Locate every blood parasite and identify its species.
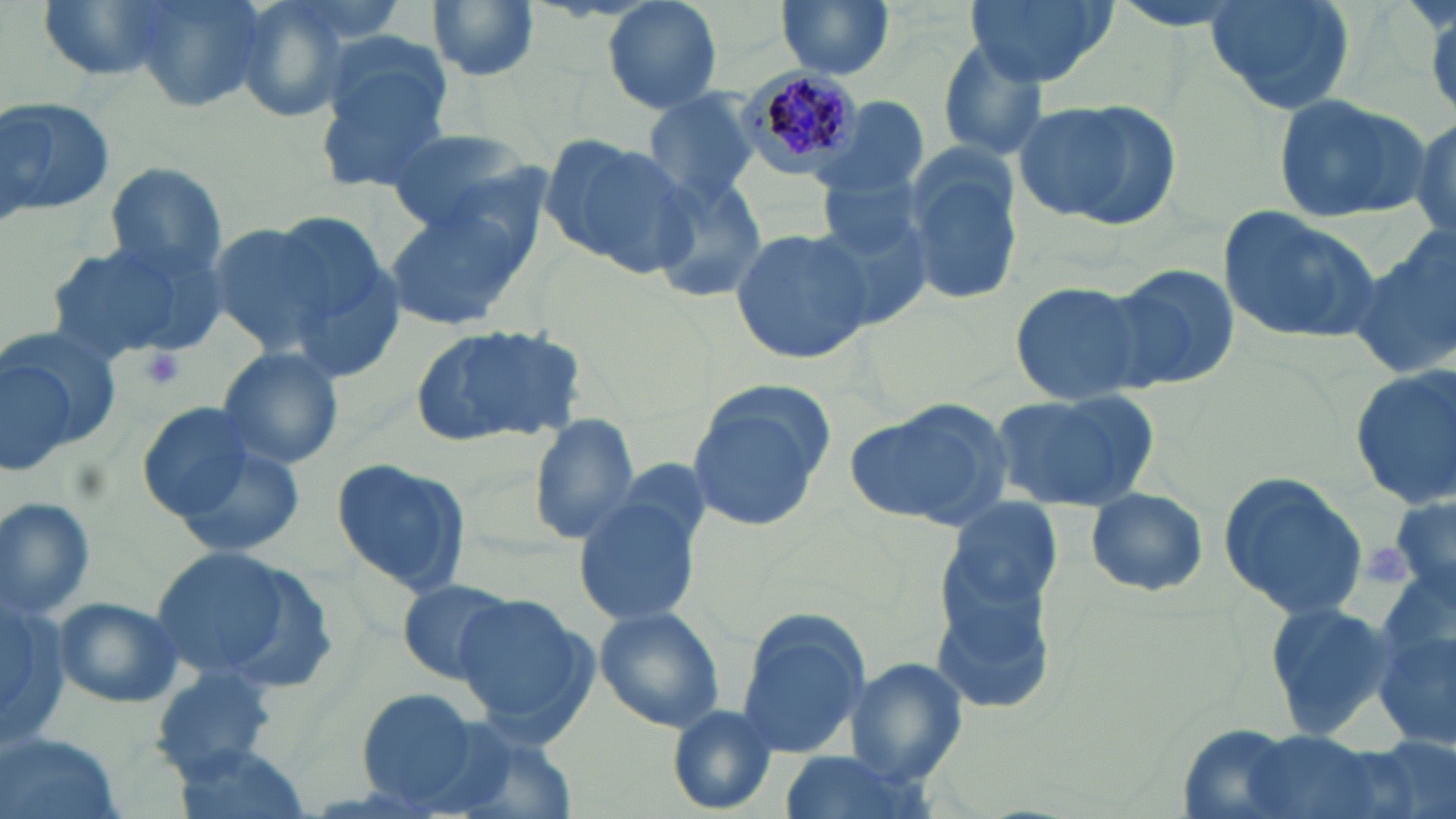

Approximate bounding boxes as (x1, y1, x2, y2) in pixels.
Plasmodium malariae-infected red blood cells: (735, 67, 864, 182).
No Plasmodium falciparum, Plasmodium ovale, Plasmodium vivax, Babesia divergens, or Trypanosoma brucei observed.

Summary:
  - Uninfected red blood cell locations: (121, 0, 268, 113), (230, 0, 372, 125), (601, 0, 723, 115), (776, 0, 893, 81), (961, 0, 1118, 88), (1204, 0, 1356, 116), (424, 1, 542, 84), (314, 36, 453, 171), (937, 40, 1049, 163), (642, 88, 762, 205), (1274, 92, 1434, 221), (1, 96, 118, 221), (816, 96, 929, 201), (1016, 96, 1184, 233), (1408, 114, 1454, 245), (383, 124, 538, 232), (541, 132, 700, 280), (905, 148, 1023, 303), (101, 163, 227, 283), (646, 166, 768, 304), (816, 166, 931, 267), (379, 196, 536, 335), (1216, 204, 1385, 347), (216, 209, 396, 364), (806, 215, 935, 330), (1346, 226, 1456, 381), (730, 227, 877, 365), (45, 238, 214, 364), (1102, 263, 1239, 396), (1007, 280, 1150, 407), (410, 322, 589, 449), (0, 329, 116, 469), (217, 345, 344, 469), (1348, 365, 1456, 511), (990, 388, 1159, 513), (686, 391, 830, 532), (847, 396, 1016, 532), (136, 400, 281, 533), (529, 415, 643, 544), (330, 455, 474, 596), (1217, 472, 1371, 622), (574, 487, 702, 630), (1084, 488, 1209, 598), (0, 497, 96, 621), (945, 499, 1062, 614), (146, 544, 331, 689), (934, 578, 1056, 717), (395, 580, 521, 683), (450, 590, 596, 743), (0, 595, 69, 746), (52, 596, 183, 708), (1261, 600, 1401, 742), (1372, 602, 1456, 759), (593, 607, 726, 734), (735, 607, 872, 763), (842, 657, 969, 784), (148, 666, 275, 778), (356, 689, 490, 805), (662, 706, 779, 815), (1176, 727, 1401, 819), (0, 731, 125, 819), (172, 742, 317, 819), (776, 753, 929, 819)
  - Platelet locations: (140, 344, 186, 393), (1362, 542, 1412, 590)
  - Slide-level diagnosis: Plasmodium malariae
  - Magnification: 1000x
  - Field of view: single
  - Preparation: thin blood smear
  - Image size: 1456×819 pixels
  - Modality: optical microscopy
  - Stain: May-Grünwald-Giemsa